Identify the blood parasite species.
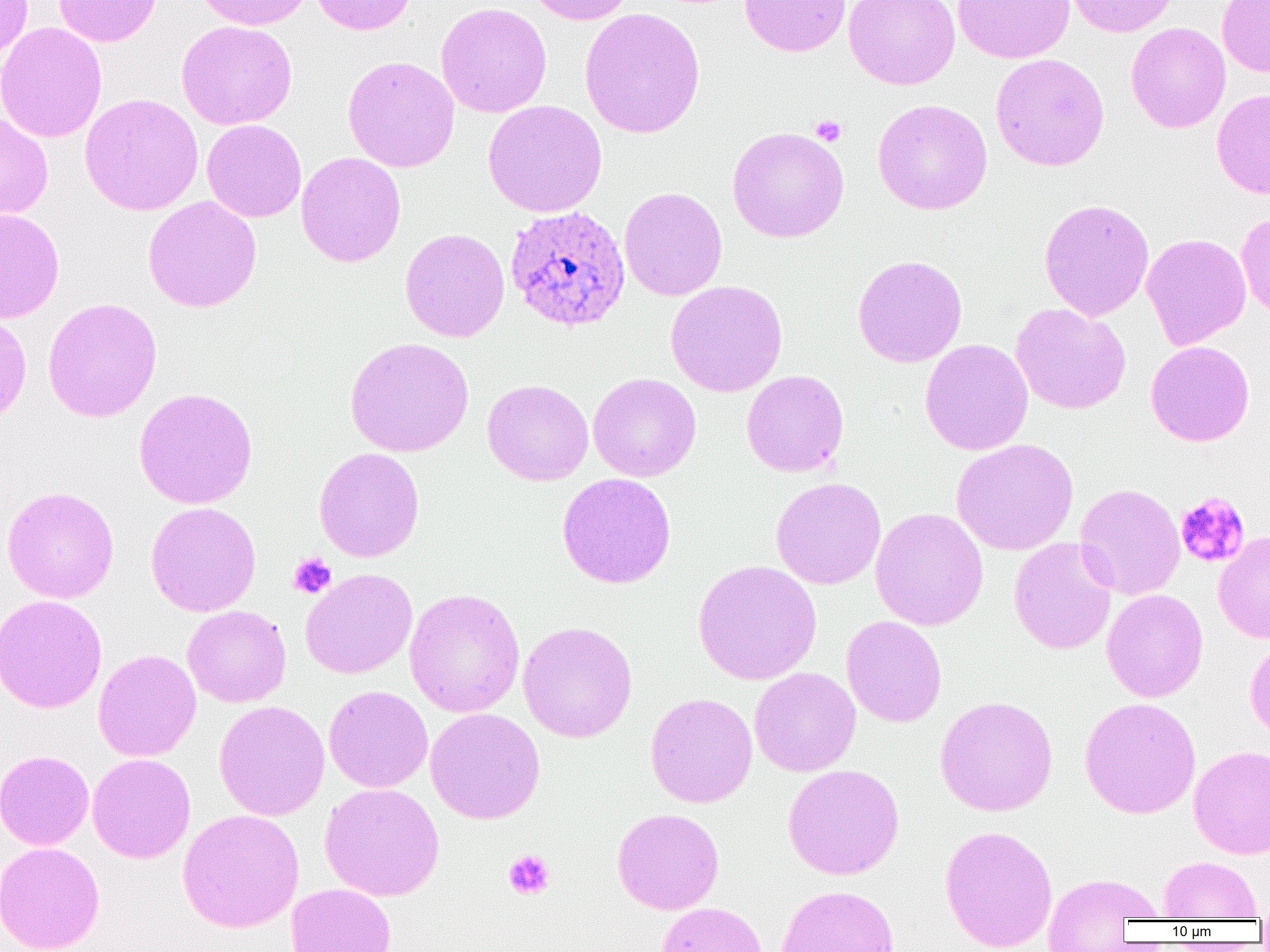

Plasmodium ovale.

Summary:
  - Coordinate format: approximate bounding boxes as (x1, y1, x2, y2) in pixels
  - Uninfected red blood cell locations: (0, 0, 32, 63), (53, 0, 161, 47), (195, 0, 313, 30), (309, 0, 417, 35), (524, 0, 637, 25), (739, 0, 851, 57), (844, 0, 960, 90), (954, 0, 1075, 63), (1065, 0, 1179, 37), (1217, 0, 1270, 77), (436, 2, 552, 117), (579, 7, 705, 139), (176, 20, 297, 130), (0, 22, 107, 143), (1126, 22, 1230, 133), (990, 53, 1110, 171), (342, 55, 459, 172), (1212, 88, 1270, 200), (80, 93, 203, 215), (872, 98, 992, 215), (483, 99, 607, 217), (0, 113, 53, 219), (202, 119, 306, 222), (727, 126, 849, 243), (296, 152, 406, 267), (619, 187, 727, 301), (143, 196, 262, 313), (1039, 198, 1154, 321), (0, 208, 64, 323), (1236, 212, 1270, 321), (400, 228, 510, 342), (1141, 233, 1251, 350), (852, 254, 967, 367), (666, 280, 788, 397), (42, 297, 162, 423), (1010, 303, 1131, 414), (0, 309, 32, 426), (344, 337, 474, 457), (920, 339, 1033, 455), (1145, 341, 1255, 446), (741, 370, 849, 477), (588, 373, 701, 481), (482, 379, 594, 486), (134, 387, 257, 509), (951, 438, 1078, 555), (313, 447, 425, 562), (557, 473, 676, 589), (770, 477, 886, 589), (1074, 483, 1185, 600), (1, 486, 119, 603), (146, 501, 261, 617), (870, 507, 988, 631), (1213, 531, 1270, 644), (1009, 538, 1117, 655), (693, 560, 821, 684), (300, 568, 418, 679), (404, 588, 525, 718), (1102, 589, 1208, 702), (0, 594, 107, 713), (182, 605, 291, 707), (841, 616, 946, 727), (518, 621, 637, 743), (1244, 635, 1270, 743), (93, 649, 201, 762), (749, 667, 861, 777), (323, 685, 433, 793), (645, 692, 757, 807), (935, 695, 1058, 816), (1080, 696, 1201, 819), (214, 700, 330, 821), (425, 708, 545, 825), (1189, 744, 1270, 859), (0, 749, 94, 850), (88, 753, 196, 863), (782, 764, 904, 880), (319, 782, 445, 901), (612, 807, 725, 914), (178, 809, 304, 933), (939, 824, 1058, 951), (0, 841, 105, 952), (1158, 856, 1263, 920), (1041, 871, 1164, 948), (286, 883, 396, 952), (775, 884, 899, 952), (656, 901, 768, 952)
  - Plasmodium ovale-infected red blood cell locations: (505, 204, 630, 332)
  - Platelet locations: (810, 114, 847, 147), (1174, 492, 1250, 568), (288, 553, 337, 599), (503, 849, 555, 900)
  - Modality: light microscopy
  - Magnification: 1000x
  - Image size: 1270×952 pixels
  - Field of view: one of a larger specimen
  - Preparation: thin blood film